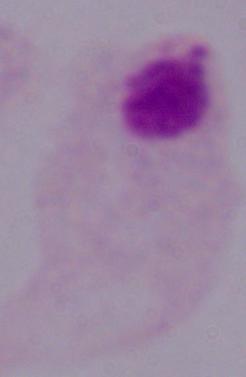

Photomicrograph. A trichomonad is seen. Captured at 1000x magnification.